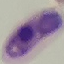
Result: malaria parasites identified. Thin blood film. Giemsa stain. Photographed with a smartphone camera at the microscope eyepiece. Cell patch, automatically extracted from a larger field of view and resized to 64 × 64 pixels.